Assess for malaria.
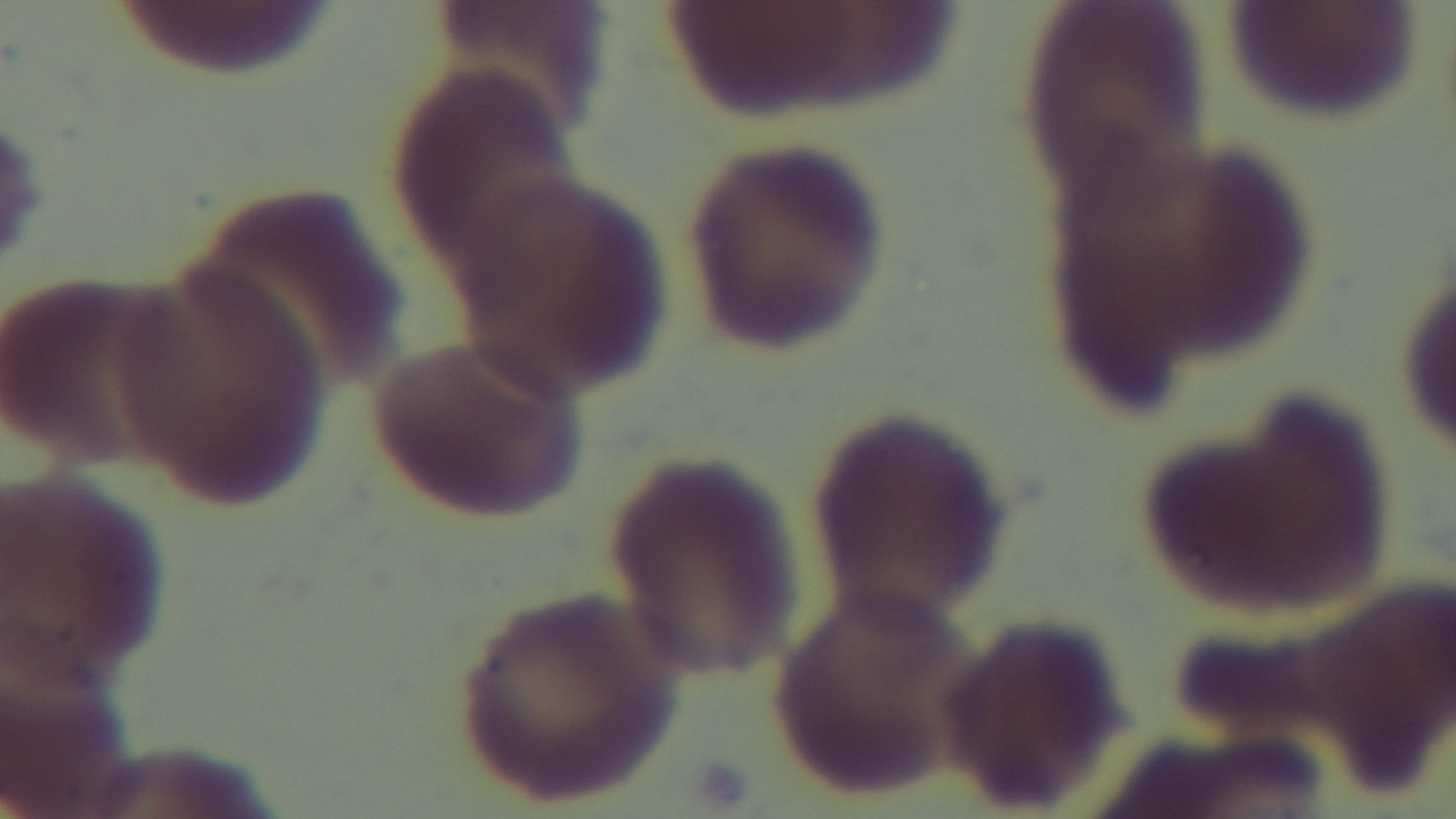

It is uninfected.

stain = Giemsa
objective = 100x oil immersion
capture = mounted 4K digital camera
preparation = thin smear
modality = light microscopy
field of view = one from the slide